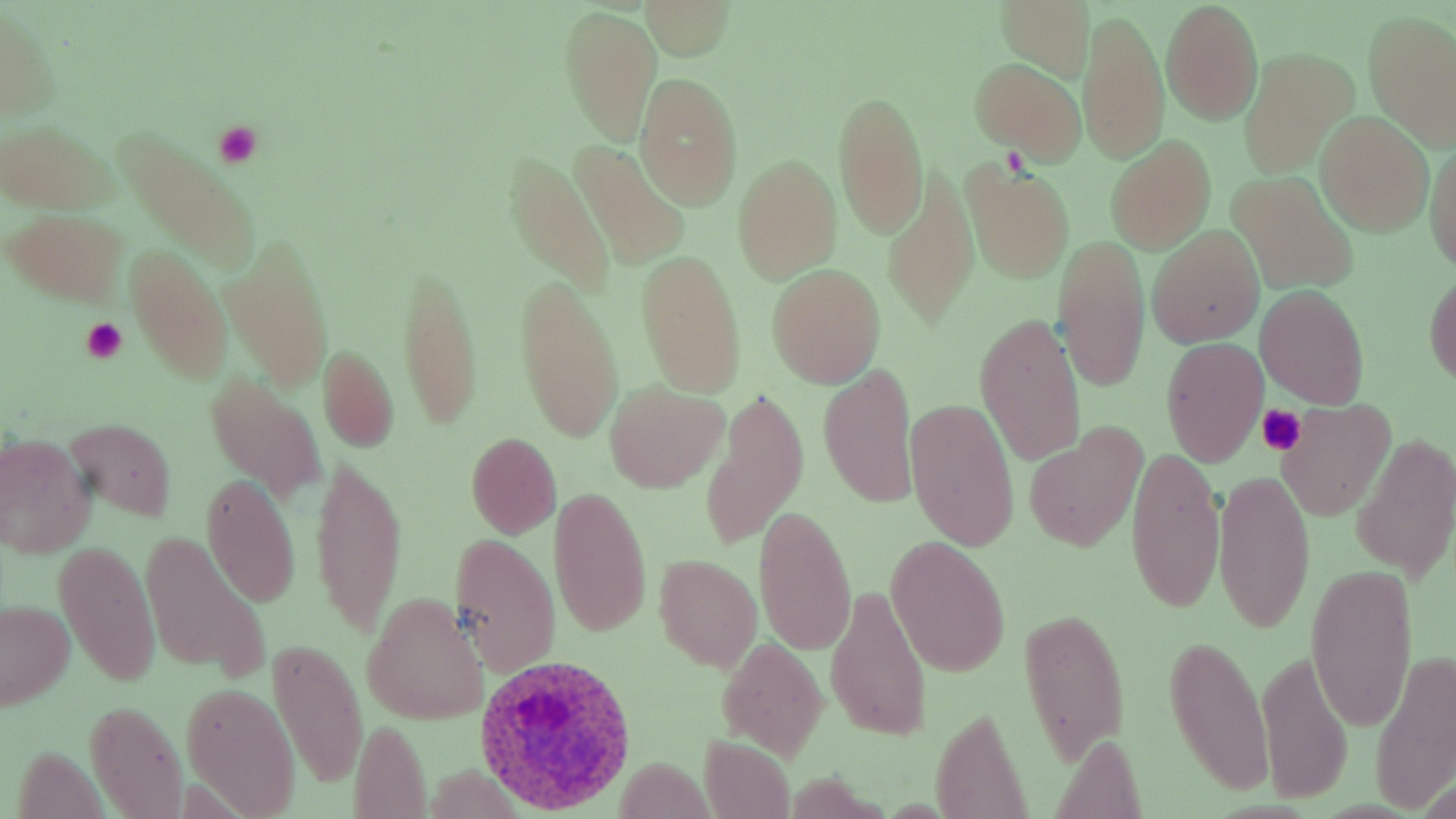
slide-level diagnosis = Plasmodium ovale
field of view = single
preparation = thin blood smear
stain = May-Grünwald-Giemsa
image size = 1456×819 pixels
Plasmodium ovale-infected red blood cell locations = approximate bounding boxes as (x1,y1)-(x2,y2) corner pairs in pixels: (474,654)-(639,815)
modality = light microscopy
platelet locations = approximate bounding boxes as (x1,y1)-(x2,y2) corner pairs in pixels: (212,121)-(262,167), (80,316)-(129,362), (1255,403)-(1308,456)
uninfected red blood cell locations = approximate bounding boxes as (x1,y1)-(x2,y2) corner pairs in pixels: (643,1)-(733,60), (996,2)-(1095,81), (1161,2)-(1263,123), (0,5)-(59,124), (561,5)-(660,145), (1078,11)-(1169,165), (1362,12)-(1456,151), (1239,49)-(1356,177), (969,59)-(1085,160), (634,73)-(744,208), (833,90)-(929,239), (1315,112)-(1432,234), (2,122)-(112,215), (113,127)-(263,271), (1425,132)-(1456,276), (1105,136)-(1217,253), (573,142)-(687,269), (503,155)-(613,295), (732,155)-(841,283), (963,161)-(1075,283), (882,168)-(976,329), (1230,173)-(1357,293), (6,207)-(129,308), (1147,226)-(1264,347), (1052,234)-(1150,392), (223,237)-(332,387), (125,246)-(234,381), (636,250)-(748,398), (397,261)-(482,431), (768,264)-(885,386), (1425,272)-(1456,387), (514,273)-(624,444), (1256,285)-(1369,408), (974,312)-(1087,468), (1160,337)-(1268,466), (317,345)-(399,453), (819,364)-(919,506), (205,374)-(325,501), (604,380)-(726,492), (700,389)-(807,549), (905,397)-(1020,553), (1276,400)-(1396,520), (64,417)-(176,522), (1023,427)-(1148,550), (0,433)-(95,557), (465,433)-(563,538), (1352,436)-(1454,581), (1125,444)-(1225,616), (311,453)-(405,640), (1212,469)-(1315,633), (202,473)-(301,606), (548,487)-(651,638), (755,506)-(857,655), (449,531)-(561,676), (143,534)-(270,679), (53,537)-(162,690), (886,538)-(1011,676), (654,555)-(762,671), (1305,563)-(1419,732), (827,583)-(932,741), (361,593)-(488,726), (0,600)-(76,710), (1017,605)-(1130,764), (1162,633)-(1275,800), (269,636)-(366,789), (716,638)-(827,759), (1370,645)-(1456,810), (1255,646)-(1352,806), (181,682)-(300,816), (85,698)-(186,818), (928,705)-(1033,819), (349,719)-(432,818), (699,735)-(795,818), (612,758)-(717,815)
magnification = 1000x